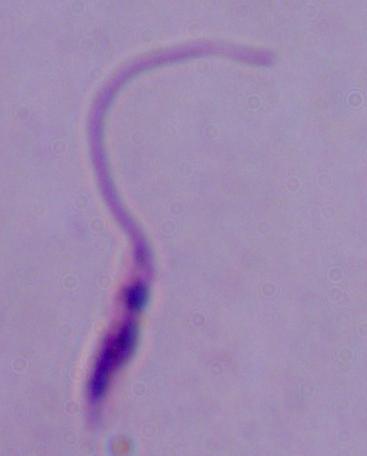

identification = Leishmania
magnification = 1000x
modality = photomicrograph